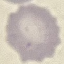

Malaria status: uninfected. Cell patch, automatically extracted from a larger field of view and resized to 64 × 64 pixels. Giemsa-stained preparation. Photographed with a smartphone camera at the microscope eyepiece. Thin blood smear.